Outline each blood parasite and name the species.
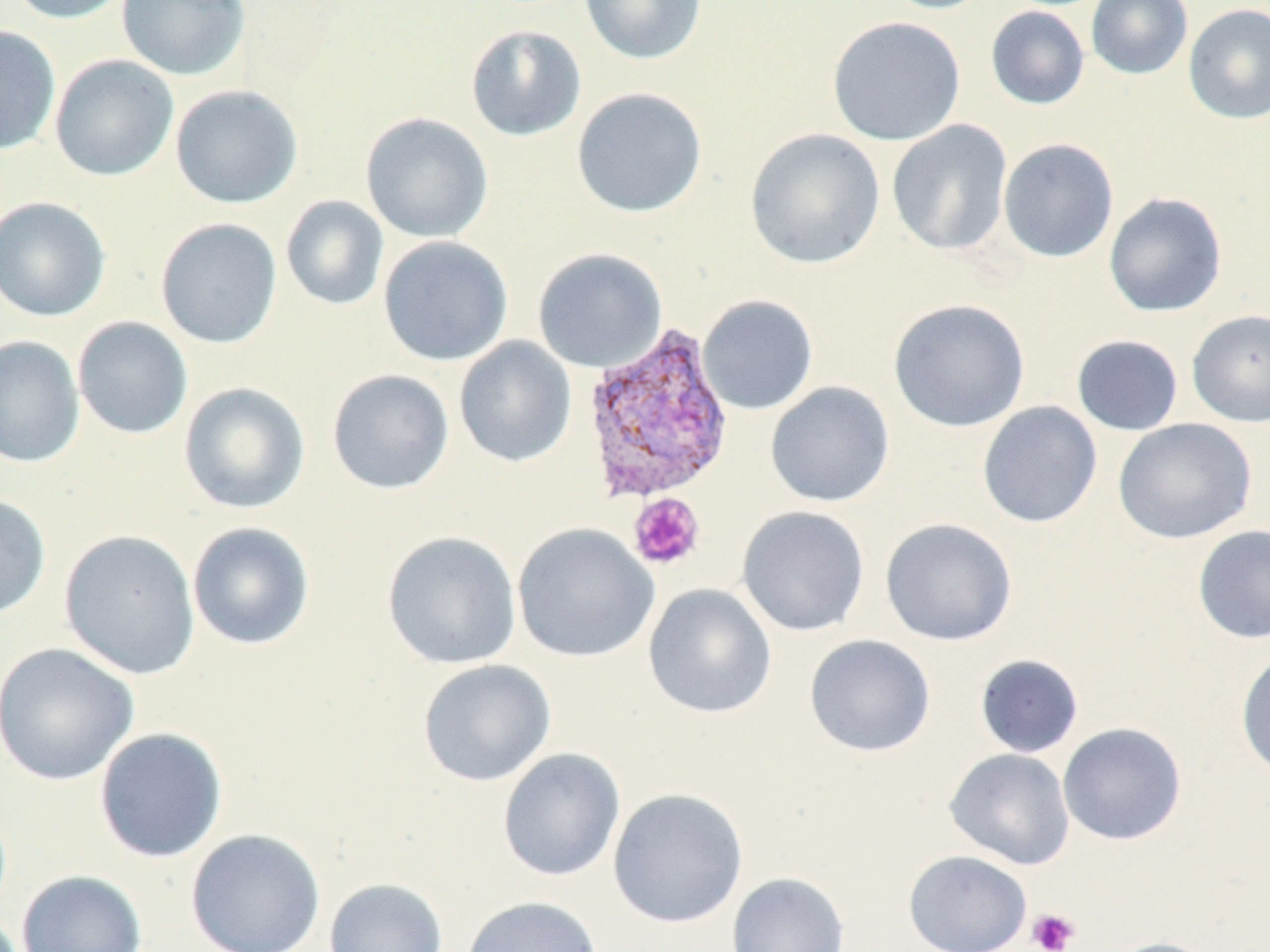

Approximate bounding boxes as [x1, y1, x2, y2] in pixels.
Plasmodium vivax-infected red blood cells: [580, 322, 736, 505].
No Plasmodium falciparum, Plasmodium ovale, Plasmodium malariae, Babesia divergens, or Trypanosoma brucei observed.

Platelet locations: [627, 493, 705, 570], [1027, 908, 1080, 952]. Uninfected red blood cell locations: [4, 0, 135, 24], [116, 0, 250, 81], [579, 0, 707, 65], [880, 0, 998, 15], [1086, 0, 1193, 80], [1184, 4, 1270, 124], [985, 5, 1090, 109], [827, 15, 966, 146], [465, 24, 587, 141], [0, 25, 61, 156], [49, 54, 179, 182], [169, 84, 303, 209], [571, 87, 708, 218], [360, 112, 494, 243], [887, 119, 1013, 256], [745, 128, 885, 269], [998, 138, 1119, 262], [1103, 192, 1227, 317], [280, 195, 389, 311], [0, 197, 111, 322], [155, 217, 283, 349], [378, 235, 513, 366], [532, 247, 667, 372], [697, 294, 818, 415], [888, 298, 1030, 433], [1186, 309, 1270, 428], [72, 316, 193, 440], [0, 334, 85, 469], [1072, 335, 1184, 436], [453, 336, 577, 467], [326, 368, 455, 494], [178, 381, 311, 514], [765, 381, 894, 507], [977, 400, 1103, 528], [1112, 417, 1257, 544], [0, 493, 51, 621], [736, 505, 870, 637], [879, 517, 1018, 646], [186, 521, 316, 651], [512, 522, 659, 663], [1192, 524, 1270, 645], [59, 529, 201, 680], [381, 530, 521, 669], [643, 583, 777, 719], [804, 634, 937, 757], [0, 642, 140, 786], [1235, 648, 1270, 780], [974, 653, 1084, 758], [417, 659, 556, 787], [1057, 722, 1186, 846], [94, 727, 228, 863], [497, 747, 625, 882], [944, 748, 1075, 870], [607, 787, 749, 928], [185, 829, 325, 952], [903, 849, 1032, 952], [15, 869, 148, 952], [726, 872, 850, 952], [324, 878, 448, 952], [461, 895, 603, 952], [1104, 936, 1220, 952]. Slide-level diagnosis: Plasmodium vivax. Captured at 1000x magnification. Light microscopy. One field of a larger specimen. May-Grünwald-Giemsa stain. Image is 1270×952 pixels. Thin blood smear.